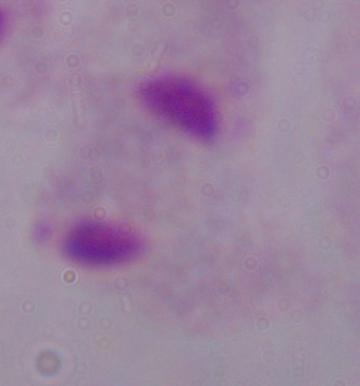
Summary:
  - Modality: photomicrograph
  - Magnification: 1000x
  - Identification: trichomonad